Assess this cell for malaria.
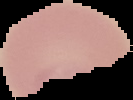

Parasitized.

From a thin blood film. Segmented cell region on a black background. Image is 133×100 pixels.